Report the malaria status of this cell.
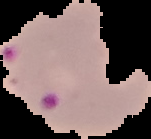

It is parasitized.

Summary:
  - Preparation: thin blood film
  - Image type: cell region segmented out of the field of view; surrounding area masked to black
  - Image size: 151×139 pixels